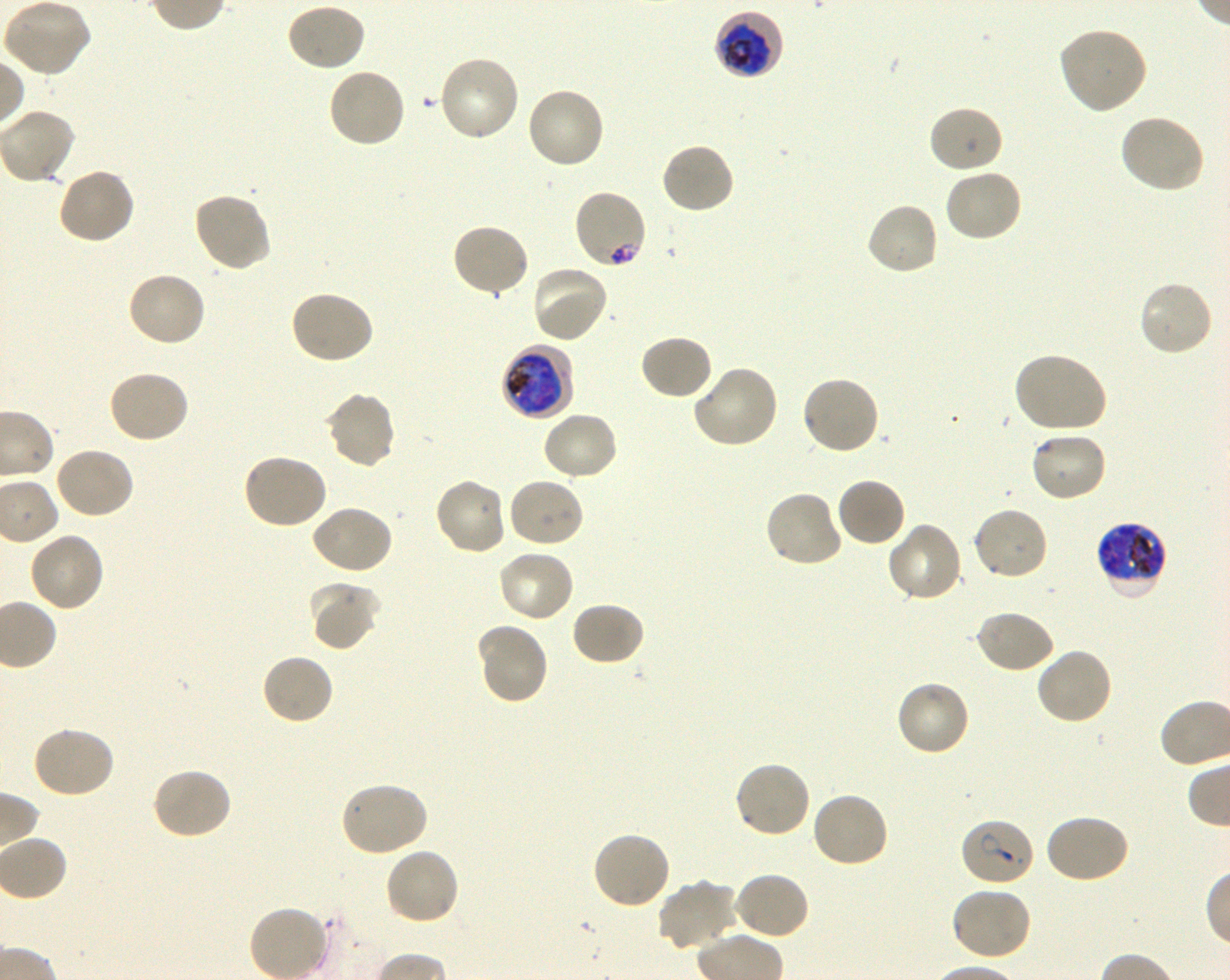

Approximate bounding rectangles given as corner coordinates in pixels from the top-left. Not every red blood cell is marked. A life-cycle stage — or a range of stages, where the recorded stages span more than one — follows each staged infected red blood cell.
Summary:
  - Locations of infected red blood cells: (x1=713, y1=12, x2=785, y2=78) early trophozoite to late schizont; (x1=501, y1=342, x2=573, y2=421) early trophozoite to late schizont; (x1=1095, y1=521, x2=1169, y2=600) late trophozoite to late schizont; (x1=959, y1=817, x2=1036, y2=888)
  - Locations of red blood cells of indeterminate infection status: (x1=572, y1=189, x2=650, y2=270)
  - Locations of uninfected red blood cells: (x1=285, y1=3, x2=367, y2=72), (x1=8, y1=6, x2=91, y2=75), (x1=1057, y1=27, x2=1148, y2=115), (x1=437, y1=55, x2=521, y2=143), (x1=327, y1=67, x2=407, y2=149), (x1=524, y1=86, x2=605, y2=170), (x1=927, y1=105, x2=1003, y2=175), (x1=1118, y1=113, x2=1205, y2=194), (x1=660, y1=142, x2=736, y2=216), (x1=56, y1=167, x2=135, y2=245), (x1=944, y1=168, x2=1024, y2=243), (x1=192, y1=191, x2=271, y2=274), (x1=864, y1=201, x2=939, y2=277), (x1=450, y1=223, x2=531, y2=299), (x1=530, y1=263, x2=610, y2=344), (x1=126, y1=270, x2=207, y2=348), (x1=1137, y1=279, x2=1214, y2=358), (x1=288, y1=290, x2=375, y2=365), (x1=639, y1=334, x2=714, y2=401), (x1=1012, y1=352, x2=1108, y2=434), (x1=693, y1=363, x2=781, y2=449), (x1=107, y1=369, x2=190, y2=444), (x1=800, y1=376, x2=880, y2=456), (x1=323, y1=391, x2=397, y2=471), (x1=540, y1=410, x2=619, y2=482), (x1=1028, y1=430, x2=1108, y2=503), (x1=52, y1=446, x2=135, y2=520), (x1=242, y1=453, x2=329, y2=531), (x1=433, y1=476, x2=507, y2=555), (x1=506, y1=476, x2=585, y2=548), (x1=835, y1=477, x2=906, y2=548), (x1=763, y1=490, x2=842, y2=569), (x1=310, y1=504, x2=394, y2=575), (x1=972, y1=506, x2=1049, y2=582), (x1=885, y1=522, x2=965, y2=603), (x1=27, y1=532, x2=105, y2=614), (x1=496, y1=547, x2=575, y2=623), (x1=308, y1=583, x2=381, y2=651), (x1=570, y1=601, x2=646, y2=667), (x1=974, y1=608, x2=1056, y2=675), (x1=476, y1=622, x2=550, y2=705), (x1=1034, y1=646, x2=1113, y2=727), (x1=261, y1=653, x2=336, y2=727), (x1=895, y1=680, x2=972, y2=758), (x1=29, y1=725, x2=116, y2=800), (x1=733, y1=760, x2=812, y2=840), (x1=151, y1=767, x2=234, y2=841), (x1=340, y1=780, x2=429, y2=858), (x1=809, y1=790, x2=889, y2=869), (x1=1043, y1=812, x2=1130, y2=884), (x1=591, y1=831, x2=673, y2=910), (x1=383, y1=846, x2=461, y2=926), (x1=733, y1=871, x2=810, y2=941), (x1=657, y1=879, x2=739, y2=952), (x1=950, y1=886, x2=1033, y2=963), (x1=247, y1=904, x2=330, y2=980)
  - Preparation: thin blood smear
  - Objective: 100x, oil immersion, numerical aperture 1.30
  - Culture: in-vitro Plasmodium falciparum strain 3D7, shaking
  - Stain: Giemsa
  - Field of view: one from this slide
  - Image size: 1230×980 pixels
  - Donor blood group: O+